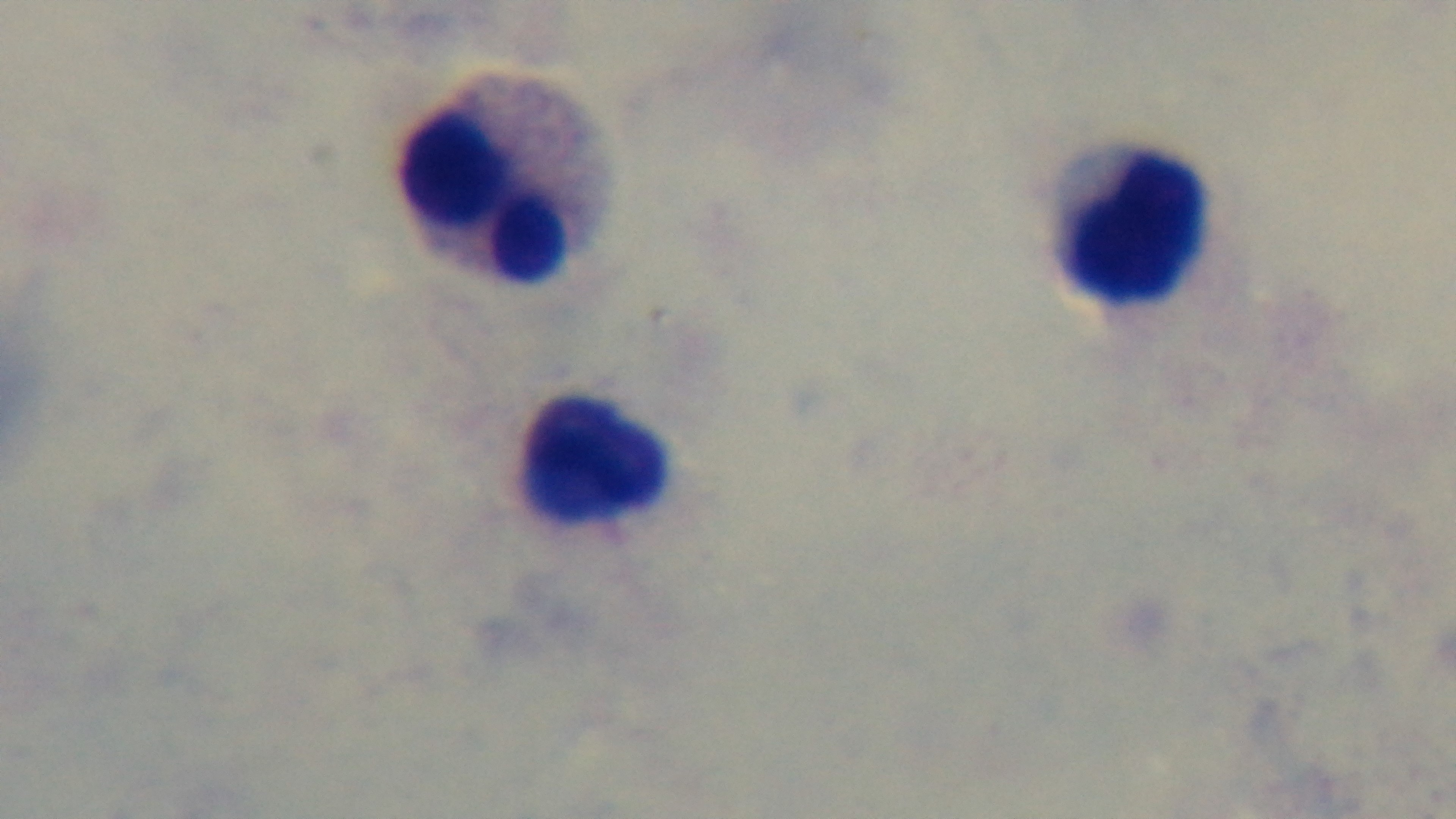
modality = light microscopy
capture = mounted 4K digital camera
field of view = single
objective = 100x oil immersion
malaria status = uninfected
stain = Giemsa
preparation = thick smear